State which parasite is depicted.
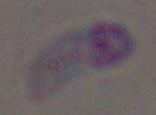

Toxoplasma gondii.

modality: photomicrograph
magnification: 1000x